Classify this cell by malaria status.
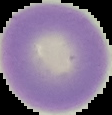

Uninfected.

Segmented cell region on a black background. Image is 112×115 pixels. From a thin blood film.